Assess this cell for malaria.
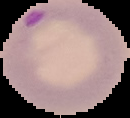
It is parasitized.

The area outside the segmented cell region is set to black. Image is 130×118 pixels. From a thin blood film.